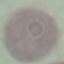

result = no malaria parasites seen
stain = Giemsa
capture = smartphone camera at the microscope eyepiece
preparation = thin blood smear
image type = automatically extracted cell patch, resized to 64 × 64 pixels